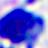
Captured at 400x magnification. Photomicrograph. A white blood cell is shown.